Report the malaria status of this cell.
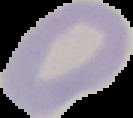
Uninfected.

{
  "preparation": "thin blood smear",
  "image_size": "133×118 pixels",
  "image_type": "cell region segmented out of the field of view; surrounding area masked to black"
}